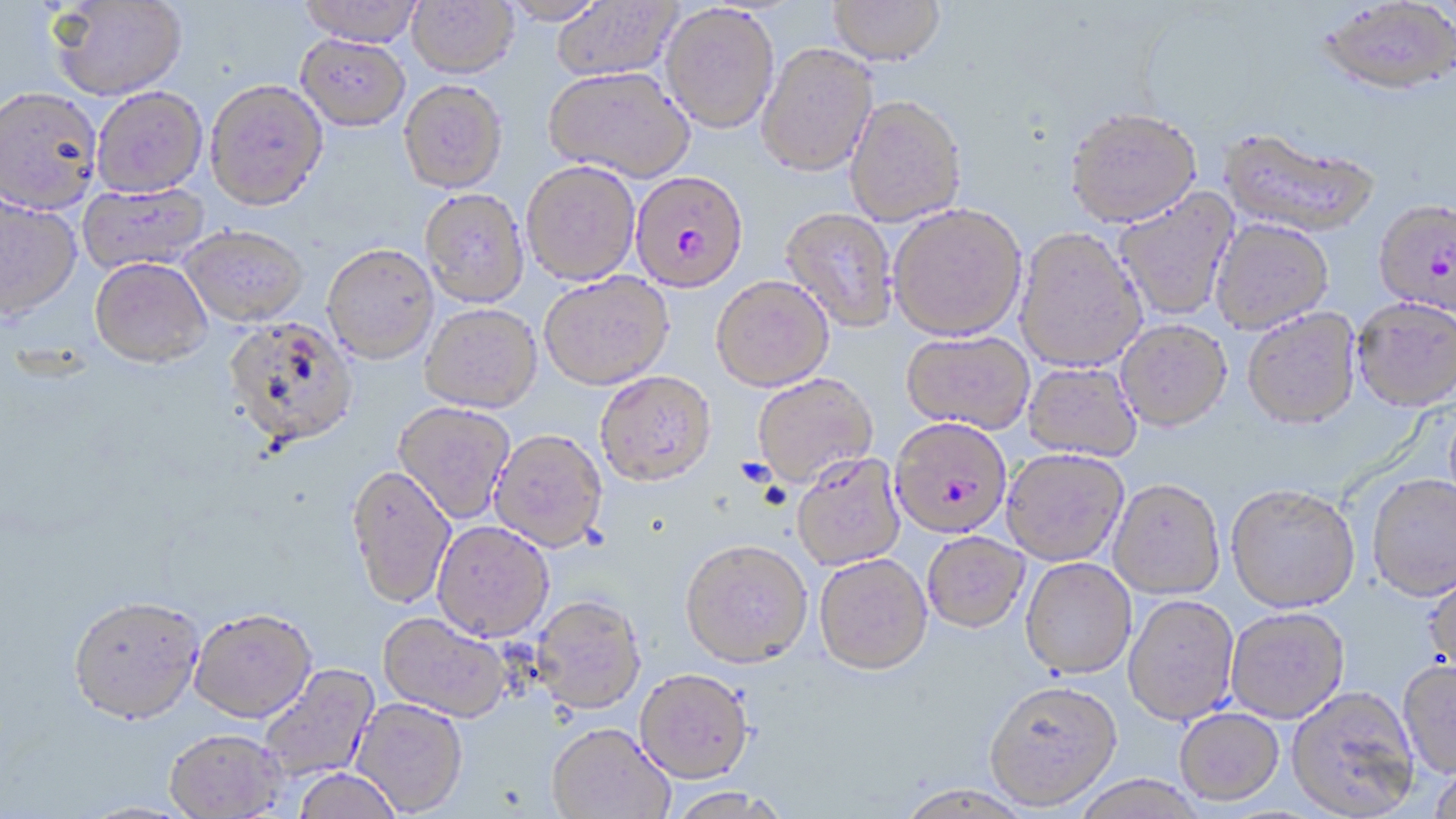

Approximate bounding boxes as [x1, y1, x2, y2] in pixels. Plasmodium falciparum-infected red blood cell locations: [630, 170, 749, 293], [1373, 201, 1456, 317], [891, 419, 1012, 542]. Uninfected red blood cell locations: [299, 0, 423, 46], [496, 0, 609, 25], [551, 0, 682, 82], [827, 0, 945, 66], [1319, 0, 1456, 99], [47, 1, 187, 100], [407, 1, 517, 78], [660, 3, 780, 133], [295, 34, 410, 131], [756, 43, 878, 178], [544, 66, 694, 181], [205, 79, 328, 210], [399, 80, 508, 193], [0, 86, 102, 214], [92, 86, 207, 197], [845, 95, 968, 226], [1065, 107, 1202, 228], [1219, 129, 1379, 239], [521, 160, 640, 285], [77, 183, 210, 274], [1113, 188, 1239, 322], [419, 189, 529, 307], [0, 195, 81, 321], [888, 205, 1026, 341], [780, 207, 899, 332], [1210, 219, 1334, 334], [181, 226, 309, 326], [1015, 228, 1146, 373], [322, 243, 439, 364], [90, 257, 212, 367], [539, 272, 674, 391], [710, 274, 834, 393], [1352, 298, 1456, 413], [420, 303, 542, 413], [1243, 309, 1361, 431], [223, 317, 359, 449], [1116, 320, 1232, 432], [901, 331, 1034, 435], [1022, 362, 1141, 463], [594, 371, 716, 488], [752, 374, 878, 489], [393, 402, 515, 524], [489, 429, 608, 552], [1001, 450, 1128, 567], [792, 454, 906, 571], [345, 464, 456, 610], [1367, 475, 1456, 603], [1108, 480, 1225, 601], [1226, 486, 1360, 614], [432, 521, 554, 642], [922, 532, 1031, 635], [680, 541, 813, 670], [814, 554, 933, 677], [1020, 558, 1137, 680], [1423, 566, 1456, 680], [1123, 595, 1240, 726], [530, 596, 646, 715], [68, 598, 205, 729], [188, 609, 317, 726], [1225, 609, 1349, 724], [377, 611, 511, 723], [1397, 661, 1456, 780], [259, 664, 379, 783], [635, 669, 754, 784], [983, 680, 1122, 811], [1286, 688, 1420, 818], [351, 698, 468, 816], [1175, 708, 1285, 807], [547, 724, 674, 819], [163, 731, 288, 819], [1427, 765, 1456, 818], [293, 769, 402, 819], [1072, 776, 1208, 819], [894, 784, 1035, 819], [667, 786, 788, 818]. Slide-level diagnosis: Plasmodium falciparum. One field of a larger specimen. Captured at 1000x magnification. Thin blood film. Image is 1456×819 pixels. Light microscopy. May-Grünwald-Giemsa-stained preparation.